Classify this cell by malaria status.
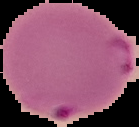
Parasitized.

The area outside the segmented cell region is set to black. Image is 139×127 pixels. From a thin blood film.